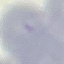
Summary:
  - Result: no malaria parasites detected
  - Capture: smartphone through the microscope eyepiece
  - Image type: cell patch, automatically extracted from a larger field of view and resized to 64 × 64 pixels
  - Stain: Giemsa
  - Preparation: thin smear